Outline each Plasmodium falciparum-infected red blood cell.
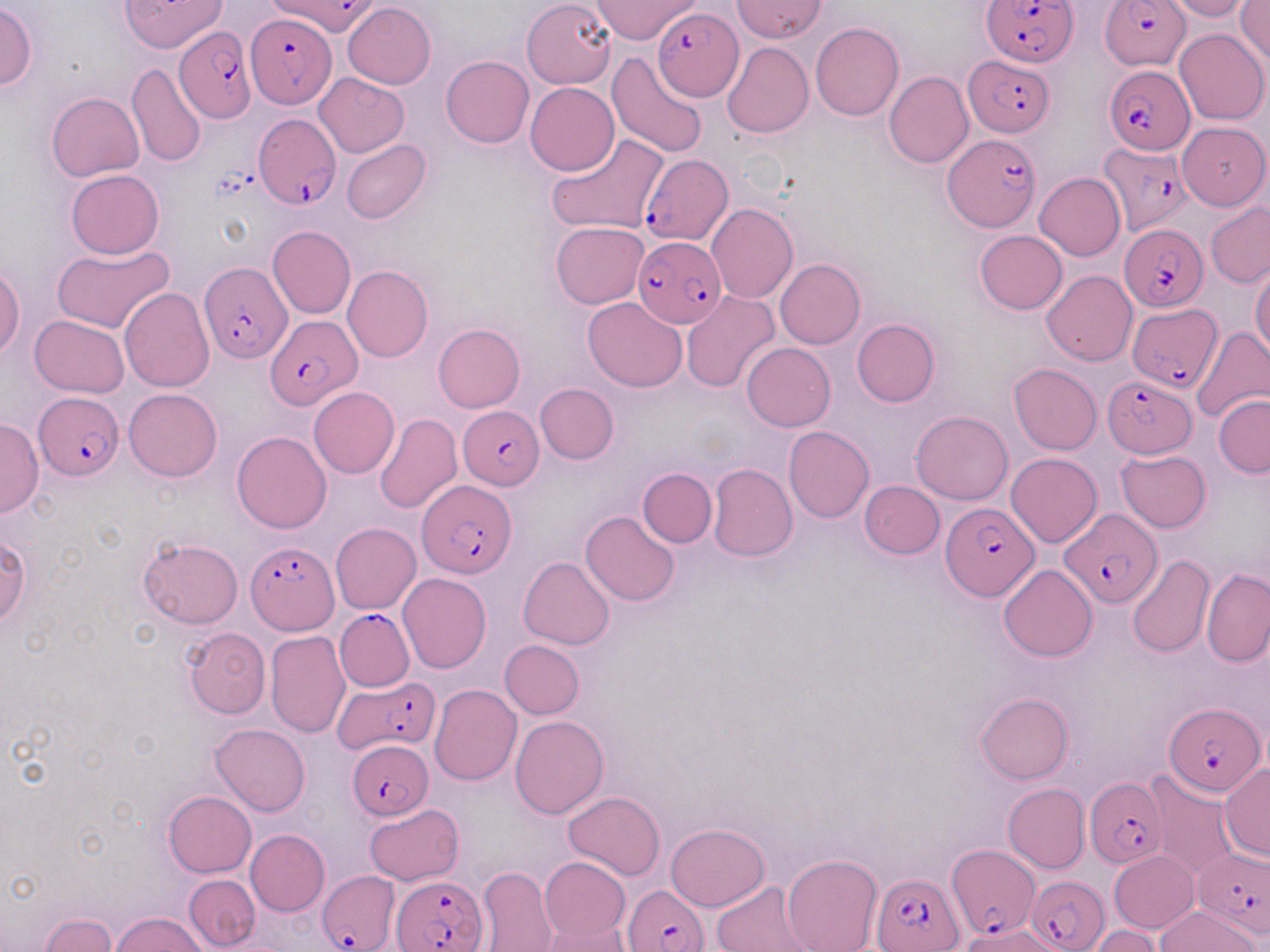

Approximate bounding boxes as named x1/y1/x2/y2 corners in pixels.
Plasmodium falciparum-infected red blood cells (subset): (x1=265, y1=0, x2=381, y2=37), (x1=983, y1=0, x2=1078, y2=67), (x1=1102, y1=0, x2=1193, y2=69), (x1=653, y1=8, x2=742, y2=100), (x1=247, y1=10, x2=334, y2=109), (x1=174, y1=26, x2=257, y2=122), (x1=964, y1=55, x2=1054, y2=136), (x1=1104, y1=66, x2=1195, y2=155), (x1=252, y1=113, x2=340, y2=211), (x1=943, y1=133, x2=1039, y2=232), (x1=1098, y1=145, x2=1193, y2=235), (x1=640, y1=153, x2=733, y2=244), (x1=1118, y1=222, x2=1207, y2=313), (x1=632, y1=235, x2=725, y2=327), (x1=199, y1=260, x2=292, y2=363), (x1=1128, y1=303, x2=1222, y2=391), (x1=265, y1=316, x2=360, y2=409), (x1=1102, y1=376, x2=1197, y2=457), (x1=33, y1=391, x2=124, y2=479), (x1=461, y1=409, x2=545, y2=489), (x1=418, y1=480, x2=516, y2=579), (x1=941, y1=502, x2=1038, y2=600), (x1=1060, y1=508, x2=1163, y2=607), (x1=245, y1=540, x2=339, y2=635), (x1=334, y1=609, x2=414, y2=691), (x1=336, y1=673, x2=442, y2=753), (x1=1164, y1=702, x2=1267, y2=798), (x1=346, y1=740, x2=435, y2=820), (x1=1085, y1=777, x2=1166, y2=870), (x1=1194, y1=848, x2=1270, y2=937), (x1=318, y1=870, x2=400, y2=951), (x1=871, y1=870, x2=963, y2=951), (x1=393, y1=875, x2=487, y2=952), (x1=1026, y1=875, x2=1108, y2=952), (x1=623, y1=883, x2=711, y2=952).

Summary:
  - Uninfected red blood cell locations (subset): (x1=119, y1=0, x2=227, y2=52), (x1=593, y1=0, x2=702, y2=44), (x1=733, y1=0, x2=827, y2=43), (x1=1165, y1=0, x2=1254, y2=21), (x1=1236, y1=1, x2=1270, y2=67), (x1=0, y1=2, x2=38, y2=91), (x1=342, y1=3, x2=435, y2=89), (x1=523, y1=4, x2=619, y2=96), (x1=812, y1=22, x2=903, y2=121), (x1=1175, y1=28, x2=1268, y2=124), (x1=723, y1=42, x2=813, y2=139), (x1=607, y1=51, x2=710, y2=158), (x1=441, y1=55, x2=534, y2=148), (x1=127, y1=64, x2=206, y2=169), (x1=884, y1=71, x2=973, y2=168), (x1=313, y1=73, x2=408, y2=156), (x1=525, y1=83, x2=619, y2=176), (x1=47, y1=92, x2=144, y2=182), (x1=1177, y1=122, x2=1268, y2=210), (x1=547, y1=132, x2=668, y2=235), (x1=342, y1=139, x2=430, y2=224), (x1=65, y1=170, x2=163, y2=259), (x1=1035, y1=173, x2=1125, y2=260), (x1=1205, y1=202, x2=1270, y2=288), (x1=706, y1=203, x2=798, y2=305), (x1=550, y1=221, x2=650, y2=309), (x1=267, y1=226, x2=356, y2=320), (x1=975, y1=230, x2=1067, y2=314), (x1=52, y1=243, x2=175, y2=333), (x1=775, y1=258, x2=865, y2=349), (x1=0, y1=262, x2=24, y2=358), (x1=343, y1=265, x2=433, y2=363), (x1=1250, y1=265, x2=1270, y2=359), (x1=1041, y1=270, x2=1137, y2=367), (x1=120, y1=288, x2=215, y2=392), (x1=681, y1=291, x2=781, y2=394), (x1=582, y1=298, x2=688, y2=392), (x1=29, y1=315, x2=130, y2=396), (x1=851, y1=318, x2=939, y2=407), (x1=433, y1=324, x2=525, y2=413), (x1=1192, y1=325, x2=1270, y2=424), (x1=742, y1=342, x2=836, y2=431), (x1=1009, y1=363, x2=1102, y2=455), (x1=534, y1=383, x2=619, y2=464), (x1=308, y1=387, x2=399, y2=478), (x1=124, y1=388, x2=221, y2=482), (x1=1214, y1=394, x2=1270, y2=477), (x1=911, y1=410, x2=1013, y2=504), (x1=375, y1=413, x2=461, y2=515), (x1=0, y1=418, x2=43, y2=517), (x1=784, y1=426, x2=874, y2=522), (x1=232, y1=431, x2=331, y2=533), (x1=1115, y1=448, x2=1211, y2=533), (x1=1006, y1=453, x2=1101, y2=547), (x1=708, y1=463, x2=798, y2=562), (x1=638, y1=467, x2=716, y2=547), (x1=859, y1=481, x2=944, y2=558), (x1=580, y1=511, x2=681, y2=607), (x1=330, y1=522, x2=421, y2=613), (x1=1, y1=535, x2=30, y2=627), (x1=136, y1=537, x2=243, y2=629), (x1=518, y1=556, x2=615, y2=649), (x1=1126, y1=556, x2=1215, y2=659), (x1=999, y1=565, x2=1096, y2=661), (x1=1202, y1=567, x2=1270, y2=666), (x1=398, y1=573, x2=491, y2=673), (x1=183, y1=626, x2=271, y2=719), (x1=266, y1=632, x2=350, y2=739), (x1=500, y1=640, x2=585, y2=719), (x1=429, y1=684, x2=521, y2=785), (x1=976, y1=691, x2=1073, y2=785), (x1=510, y1=714, x2=609, y2=818), (x1=210, y1=723, x2=311, y2=816), (x1=1218, y1=764, x2=1270, y2=861), (x1=1144, y1=770, x2=1239, y2=879), (x1=1003, y1=783, x2=1089, y2=873), (x1=563, y1=790, x2=665, y2=880), (x1=163, y1=791, x2=256, y2=877), (x1=364, y1=804, x2=464, y2=886), (x1=665, y1=823, x2=771, y2=911), (x1=246, y1=830, x2=330, y2=914), (x1=1109, y1=850, x2=1199, y2=933), (x1=781, y1=852, x2=881, y2=952), (x1=539, y1=856, x2=630, y2=944), (x1=476, y1=865, x2=558, y2=952), (x1=184, y1=874, x2=260, y2=950), (x1=712, y1=881, x2=817, y2=952), (x1=1155, y1=906, x2=1261, y2=952), (x1=112, y1=912, x2=208, y2=952), (x1=40, y1=914, x2=117, y2=951), (x1=538, y1=920, x2=630, y2=952), (x1=1090, y1=926, x2=1164, y2=952)
  - Slide-level diagnosis: Plasmodium falciparum
  - Magnification: 1000x
  - Field of view: single
  - Stain: May-Grünwald-Giemsa
  - Image size: 1270×952 pixels
  - Modality: optical microscopy
  - Preparation: thin blood film